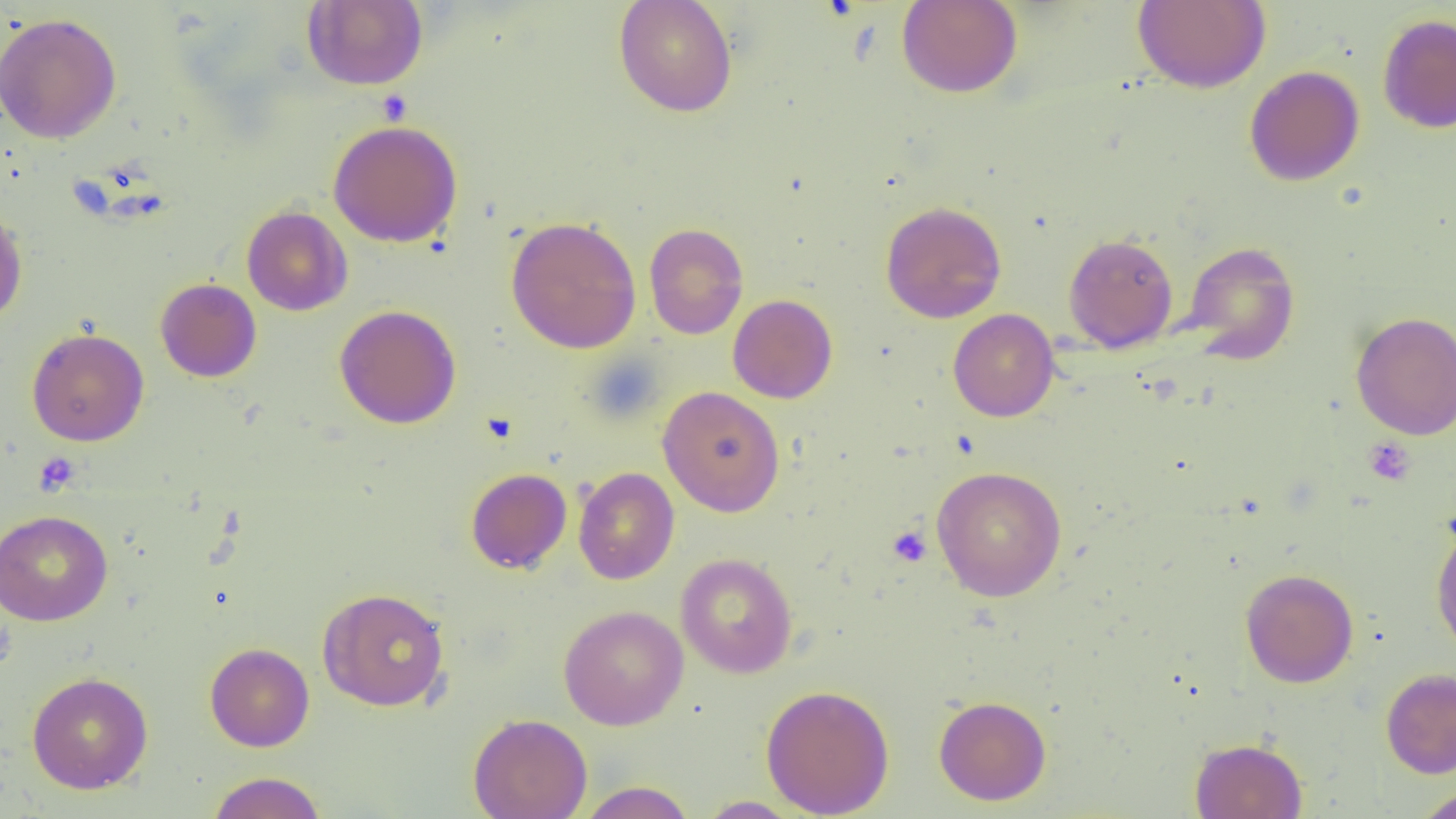
Approximate bounding boxes as (x1,y1)-(x2,y2) corner pairs in pixels. Platelet locations: (377,89)-(413,125), (1363,437)-(1416,486), (34,451)-(81,496), (887,526)-(931,567). Uninfected red blood cell locations: (302,0)-(427,90), (613,0)-(738,117), (896,0)-(1023,98), (1132,1)-(1270,93), (0,12)-(121,144), (1377,13)-(1456,134), (1244,65)-(1365,187), (328,120)-(463,248), (880,200)-(1007,324), (0,206)-(28,327), (241,206)-(353,316), (505,216)-(642,354), (644,223)-(748,339), (1063,232)-(1178,353), (1181,241)-(1301,364), (155,278)-(262,382), (728,294)-(838,403), (334,305)-(461,429), (948,308)-(1059,422), (1351,311)-(1456,439), (26,327)-(149,446), (658,386)-(785,517), (931,465)-(1067,601), (573,467)-(679,584), (465,468)-(572,574), (0,509)-(113,626), (1430,514)-(1456,659), (676,553)-(797,678), (1240,568)-(1359,688), (317,587)-(450,711), (559,605)-(689,730), (205,642)-(315,752), (1380,668)-(1456,779), (26,671)-(154,794), (760,683)-(895,817), (933,695)-(1051,805), (468,713)-(593,819), (1189,737)-(1307,819), (207,771)-(327,819), (577,781)-(696,818), (1414,787)-(1456,819), (696,796)-(804,818). Slide-level diagnosis: negative for blood parasites. Light microscopy. One field of a larger specimen. Image is 1456×819 pixels. Thin blood film. 1000x magnification.